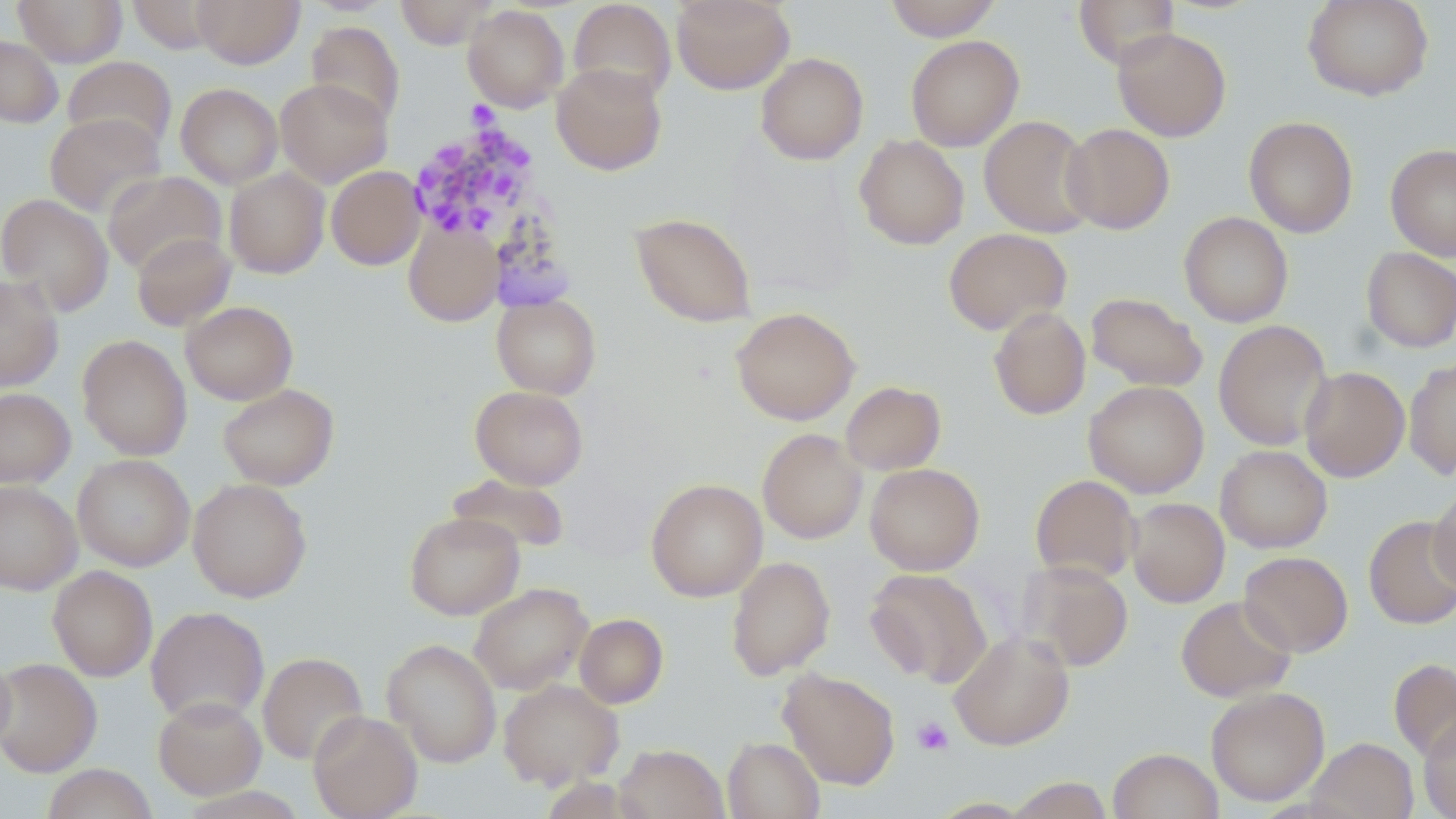
{
  "slide_level_diagnosis": "Plasmodium malariae",
  "preparation": "thin blood film",
  "magnification": "1000x",
  "plasmodium_malariae_infected_red_blood_cell_locations": "approximate bounding boxes as (x1,y1)-(x2,y2) corner pairs in pixels: (407,117)-(553,256)",
  "image_size": "1456×819 pixels",
  "modality": "optical microscopy",
  "platelet_locations": "approximate bounding boxes as (x1,y1)-(x2,y2) corner pairs in pixels: (912,717)-(954,756)",
  "stain": "May-Grünwald-Giemsa",
  "uninfected_red_blood_cell_locations": "approximate bounding boxes as (x1,y1)-(x2,y2) corner pairs in pixels: (13,0)-(128,66), (127,0)-(223,54), (192,0)-(305,68), (395,0)-(498,49), (568,0)-(676,104), (671,0)-(794,95), (882,0)-(1003,41), (1073,0)-(1179,69), (1302,0)-(1434,101), (463,5)-(569,112), (306,21)-(405,127), (1112,27)-(1231,141), (0,34)-(63,128), (905,35)-(1024,151), (755,52)-(869,165), (62,56)-(177,154), (551,62)-(667,175), (275,78)-(392,187), (175,83)-(283,188), (45,112)-(165,217), (979,115)-(1097,238), (1243,116)-(1358,238), (1061,123)-(1175,234), (854,134)-(969,250), (1385,143)-(1456,261), (326,166)-(426,270), (224,168)-(330,278), (103,171)-(226,275), (0,193)-(114,316), (1179,211)-(1293,327), (630,212)-(757,327), (403,220)-(503,327), (943,228)-(1071,335), (131,232)-(237,331), (1361,247)-(1456,352), (0,275)-(64,392), (1086,292)-(1208,392), (492,293)-(601,399), (181,301)-(298,404), (989,306)-(1091,420), (731,307)-(860,425), (1213,320)-(1333,450), (77,335)-(192,461), (1404,358)-(1456,479), (1299,366)-(1410,482), (1084,380)-(1209,497), (840,381)-(946,476), (217,383)-(339,490), (470,385)-(588,490), (0,387)-(75,488), (757,428)-(867,544), (1215,445)-(1333,553), (72,453)-(195,571), (865,463)-(985,575), (560,471)-(656,563), (445,472)-(570,555), (1030,474)-(1141,583), (187,478)-(312,602), (645,478)-(767,601), (0,480)-(82,594), (1428,486)-(1456,594), (1126,498)-(1229,607), (404,511)-(525,620), (1364,516)-(1456,629), (1239,551)-(1353,657), (726,556)-(835,680), (1018,561)-(1133,671), (48,566)-(158,681), (864,568)-(993,686), (469,582)-(592,695), (1176,596)-(1296,701), (145,606)-(270,726), (574,613)-(669,708), (949,630)-(1074,750), (382,639)-(502,768), (0,649)-(16,757), (257,651)-(369,765), (0,658)-(102,777), (1389,658)-(1456,762), (778,668)-(900,789), (498,678)-(623,789), (1206,687)-(1330,806), (153,695)-(266,799), (308,710)-(422,819), (1418,717)-(1456,818), (723,737)-(825,819), (1307,737)-(1418,819), (614,743)-(728,819), (1108,748)-(1223,819), (41,764)-(158,819), (1004,776)-(1113,818)",
  "field_of_view": "single"
}